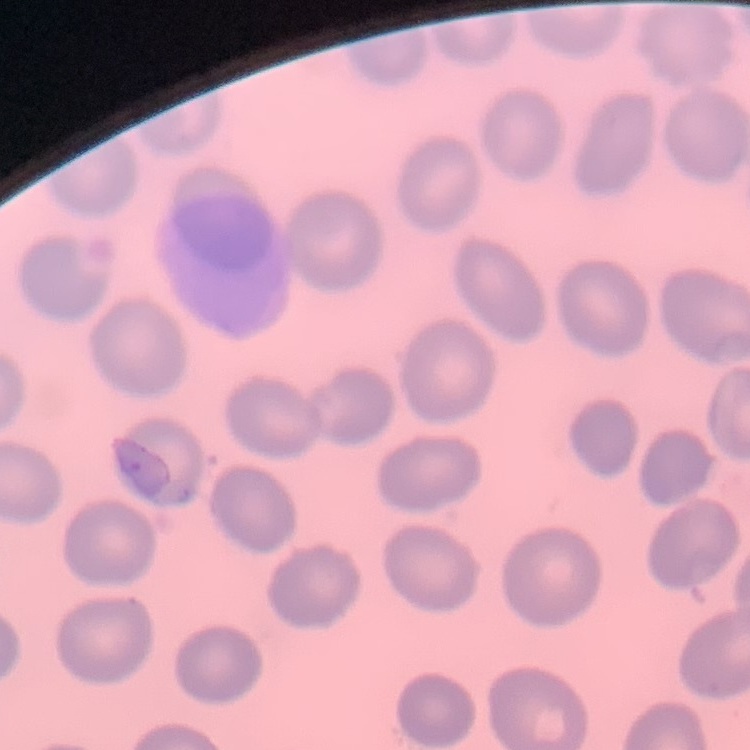

erythrocyte morphology = no rouleaux formation
preparation = thin peripheral smear
image type = square crop of a larger photomicrograph
stain = Field's or Giemsa